Assess this cell for malaria.
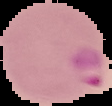

It is uninfected.

From a thin blood smear. The area outside the segmented cell region is set to black. Image is 112×106 pixels.